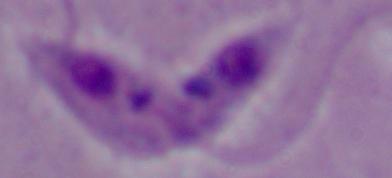

Summary:
  - Magnification: 1000x
  - Modality: micrograph
  - Identification: Leishmania